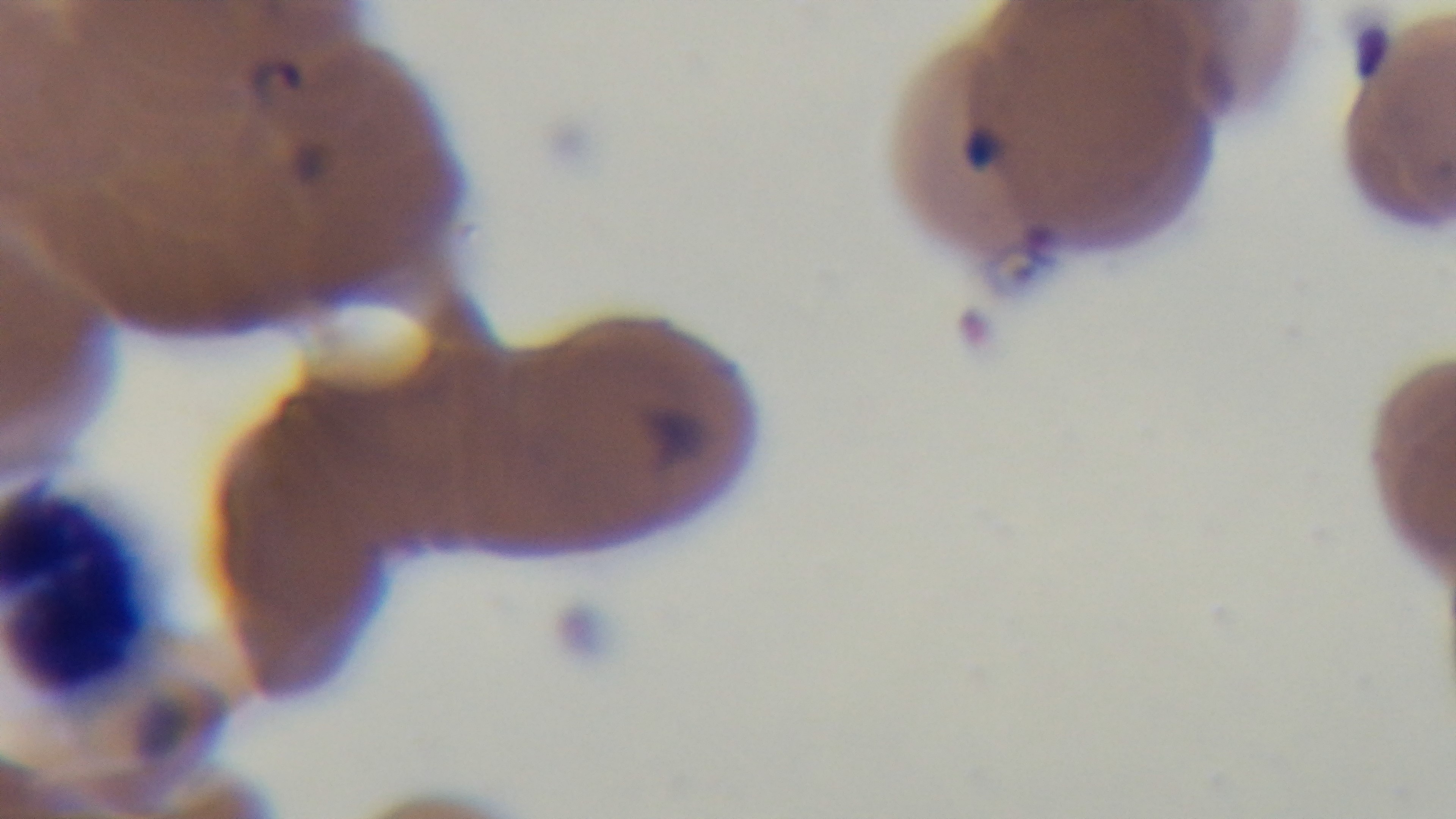 Giemsa stain. Photomicrograph. Oil-immersion objective, 100x. Malaria status: infected. Preparation: thin smear. One field from the slide. Mounted 4K digital camera.